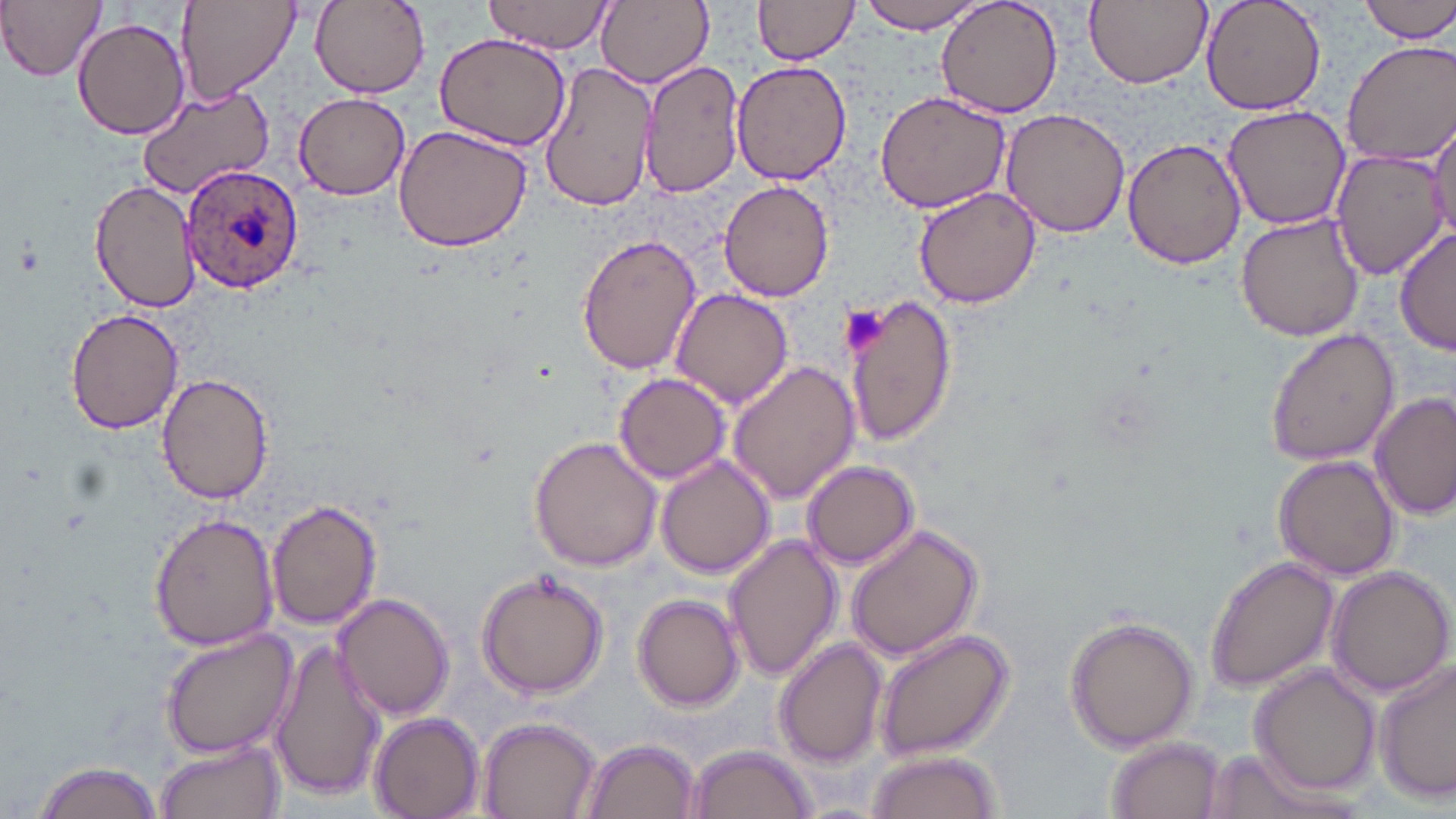
Summary:
  - Coordinate format: approximate bounding boxes as [x1, y1, x2, y2] in pixels
  - Plasmodium ovale-infected red blood cell locations: [181, 163, 303, 294]
  - Uninfected red blood cell locations: [1, 0, 107, 82], [177, 0, 301, 108], [310, 0, 428, 96], [595, 0, 714, 88], [859, 0, 988, 34], [937, 0, 1063, 119], [1086, 0, 1211, 89], [1201, 0, 1327, 114], [1361, 0, 1456, 42], [485, 1, 616, 54], [752, 1, 862, 67], [72, 16, 190, 139], [433, 30, 573, 151], [1340, 41, 1456, 167], [638, 58, 745, 199], [541, 61, 659, 213], [732, 61, 851, 186], [136, 85, 274, 200], [873, 89, 1012, 213], [293, 92, 410, 199], [1221, 102, 1351, 230], [1000, 108, 1131, 239], [1429, 109, 1456, 244], [393, 123, 534, 251], [1122, 136, 1246, 271], [1329, 149, 1449, 281], [90, 177, 203, 314], [718, 177, 834, 302], [913, 187, 1042, 311], [1237, 211, 1366, 341], [1396, 227, 1455, 360], [575, 233, 702, 375], [670, 289, 793, 408], [845, 293, 959, 446], [64, 307, 184, 435], [1264, 327, 1399, 467], [727, 359, 860, 505], [154, 372, 276, 502], [614, 373, 731, 483], [1372, 392, 1454, 522], [529, 435, 663, 572], [656, 454, 776, 578], [1273, 454, 1402, 581], [801, 461, 920, 569], [266, 499, 381, 629], [148, 510, 282, 652], [845, 523, 984, 663], [724, 532, 844, 681], [1205, 555, 1338, 694], [1326, 567, 1455, 698], [474, 568, 609, 701], [332, 592, 455, 719], [632, 594, 744, 712], [1064, 615, 1201, 754], [157, 626, 297, 760], [875, 627, 1014, 762], [269, 638, 386, 803], [774, 638, 888, 768], [1374, 659, 1455, 805], [1252, 663, 1383, 795], [371, 711, 486, 818], [480, 717, 600, 819], [1106, 737, 1225, 819], [156, 738, 285, 819], [580, 738, 699, 819], [686, 743, 817, 819], [1198, 747, 1336, 819], [867, 749, 1003, 819], [26, 758, 165, 819]
  - Platelet locations: [839, 307, 887, 355]
  - Slide-level diagnosis: Plasmodium ovale
  - Preparation: thin blood film
  - Stain: May-Grünwald-Giemsa
  - Field of view: single
  - Magnification: 1000x
  - Modality: light microscopy
  - Image size: 1456×819 pixels